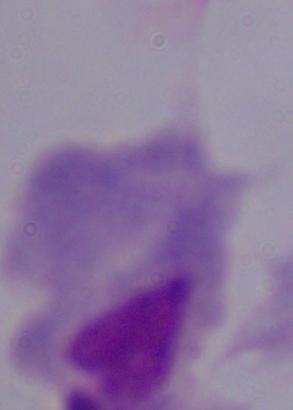

1000x magnification. A trichomonad is shown. Photomicrograph.